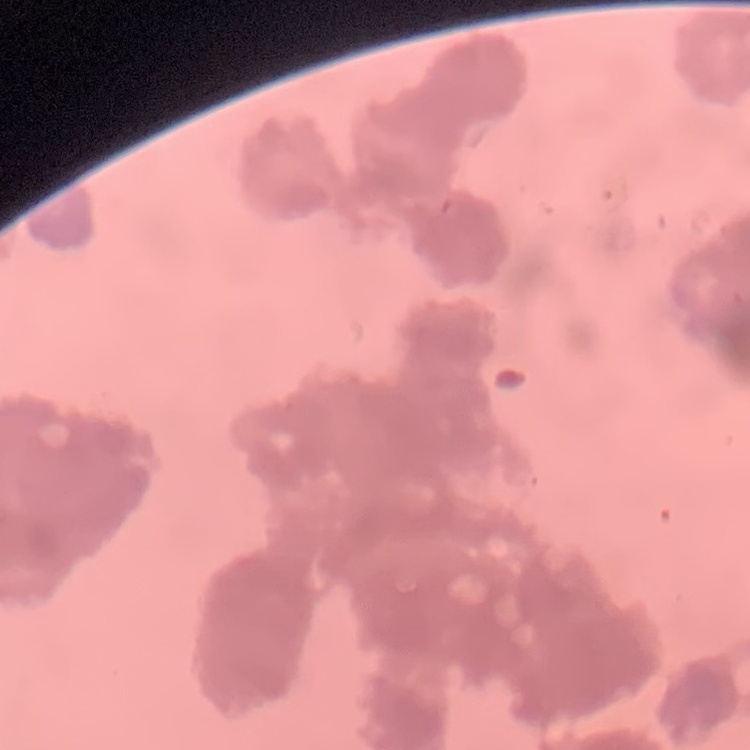 The red blood cells exhibit rouleaux formation. Stained with either Field's or Giemsa. One tile cut from a larger photomicrograph. Thin blood smear.